Report the malaria status of this cell.
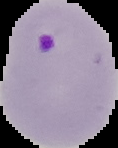
It is parasitized.

image type = cell region segmented out of the field of view; surrounding area masked to black
preparation = thin blood smear
image size = 118×148 pixels